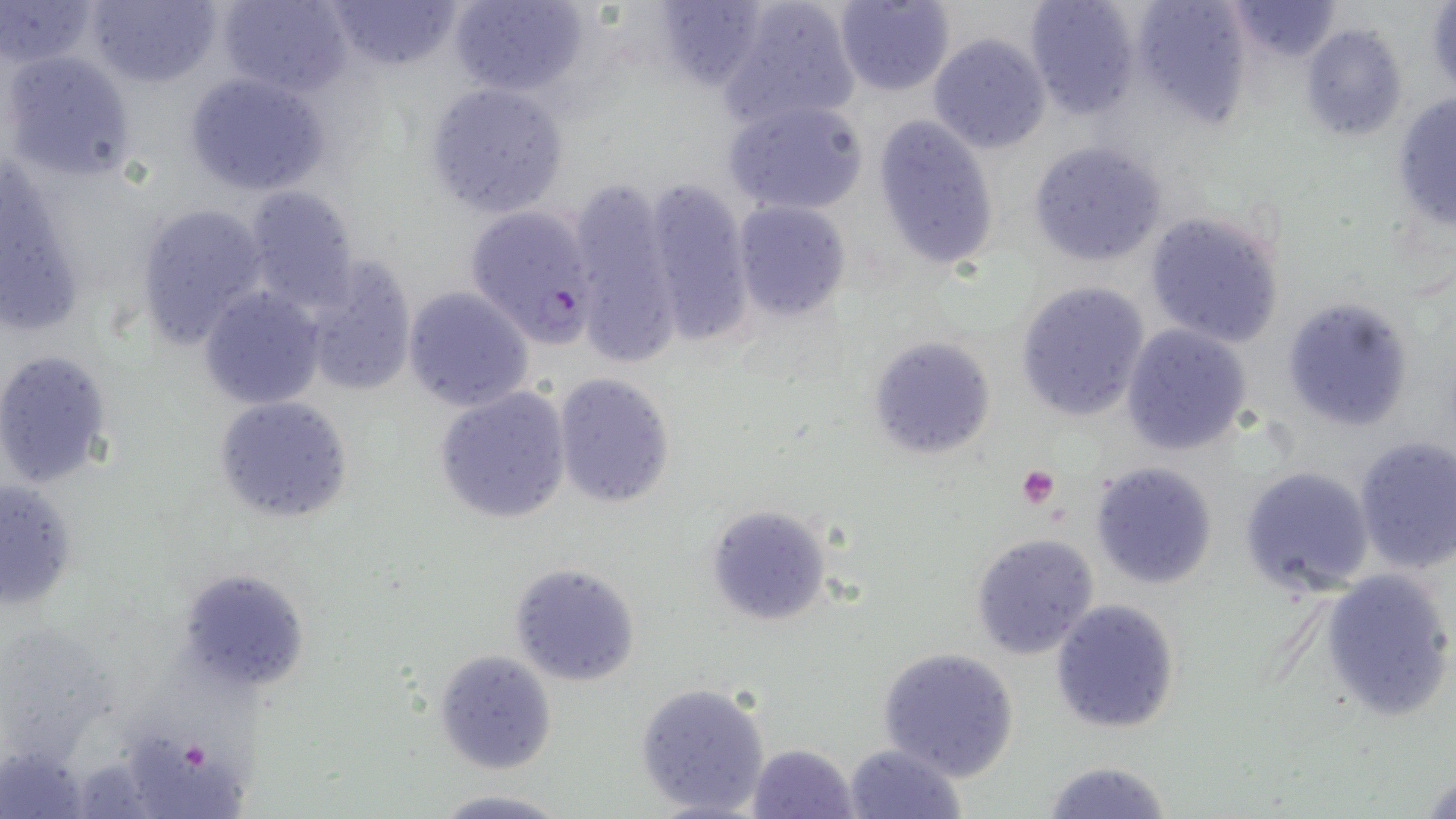

slide-level diagnosis = Plasmodium falciparum
uninfected red blood cell locations = approximate bounding boxes as named x1/y1/x2/y2 corners in pixels: (x1=3, y1=0, x2=100, y2=69), (x1=87, y1=0, x2=223, y2=89), (x1=217, y1=0, x2=351, y2=97), (x1=326, y1=0, x2=459, y2=72), (x1=446, y1=0, x2=590, y2=98), (x1=719, y1=0, x2=859, y2=127), (x1=831, y1=0, x2=955, y2=94), (x1=1023, y1=0, x2=1141, y2=119), (x1=1226, y1=0, x2=1342, y2=62), (x1=650, y1=1, x2=769, y2=91), (x1=1129, y1=1, x2=1250, y2=126), (x1=1425, y1=2, x2=1456, y2=96), (x1=1300, y1=23, x2=1408, y2=142), (x1=928, y1=33, x2=1051, y2=153), (x1=1, y1=51, x2=137, y2=184), (x1=183, y1=70, x2=331, y2=197), (x1=423, y1=84, x2=568, y2=218), (x1=1390, y1=93, x2=1456, y2=234), (x1=723, y1=97, x2=870, y2=215), (x1=871, y1=115, x2=999, y2=272), (x1=1029, y1=140, x2=1168, y2=268), (x1=1, y1=161, x2=86, y2=327), (x1=641, y1=174, x2=753, y2=342), (x1=569, y1=175, x2=688, y2=364), (x1=241, y1=184, x2=359, y2=311), (x1=132, y1=201, x2=269, y2=348), (x1=733, y1=202, x2=850, y2=319), (x1=1144, y1=210, x2=1286, y2=348), (x1=296, y1=256, x2=416, y2=396), (x1=1014, y1=281, x2=1149, y2=421), (x1=200, y1=287, x2=324, y2=410), (x1=402, y1=288, x2=533, y2=411), (x1=1279, y1=296, x2=1414, y2=432), (x1=1121, y1=324, x2=1253, y2=455), (x1=868, y1=336, x2=995, y2=461), (x1=0, y1=348, x2=117, y2=489), (x1=551, y1=372, x2=676, y2=509), (x1=433, y1=386, x2=572, y2=524), (x1=213, y1=395, x2=351, y2=522), (x1=1352, y1=435, x2=1456, y2=573), (x1=1090, y1=460, x2=1217, y2=591), (x1=1239, y1=464, x2=1375, y2=596), (x1=1, y1=478, x2=80, y2=612), (x1=704, y1=504, x2=835, y2=628), (x1=970, y1=531, x2=1101, y2=658), (x1=510, y1=562, x2=640, y2=687), (x1=1320, y1=567, x2=1455, y2=722), (x1=176, y1=568, x2=311, y2=697), (x1=1050, y1=598, x2=1182, y2=735), (x1=877, y1=646, x2=1021, y2=780), (x1=433, y1=650, x2=558, y2=773), (x1=634, y1=681, x2=771, y2=818), (x1=127, y1=736, x2=257, y2=818), (x1=842, y1=742, x2=966, y2=819), (x1=0, y1=743, x2=89, y2=819), (x1=747, y1=743, x2=859, y2=819), (x1=1040, y1=759, x2=1172, y2=819), (x1=1420, y1=763, x2=1456, y2=819), (x1=429, y1=790, x2=575, y2=819)
magnification = 1000x
modality = light microscopy
field of view = one of a larger specimen
platelet locations = approximate bounding boxes as named x1/y1/x2/y2 corners in pixels: (x1=1017, y1=466, x2=1060, y2=509)
stain = May-Grünwald-Giemsa
Plasmodium falciparum-infected red blood cell locations = approximate bounding boxes as named x1/y1/x2/y2 corners in pixels: (x1=463, y1=203, x2=601, y2=346)
image size = 1456×819 pixels
preparation = thin blood smear